Comment on the morphology of the red blood cells.
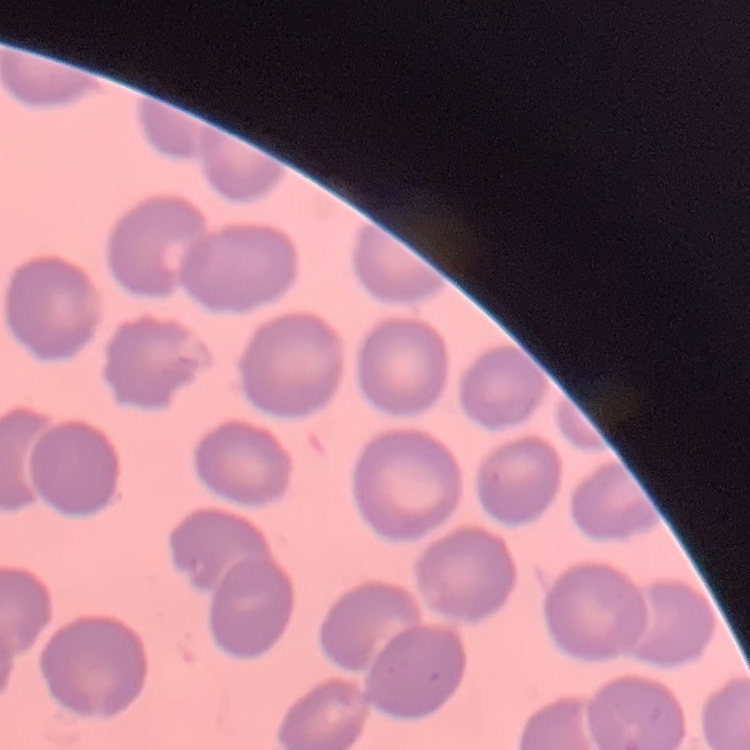

They show no rouleaux formation.

{
  "image_type": "square crop of a larger photomicrograph",
  "preparation": "thin peripheral smear",
  "stain": "Field's or Giemsa"
}